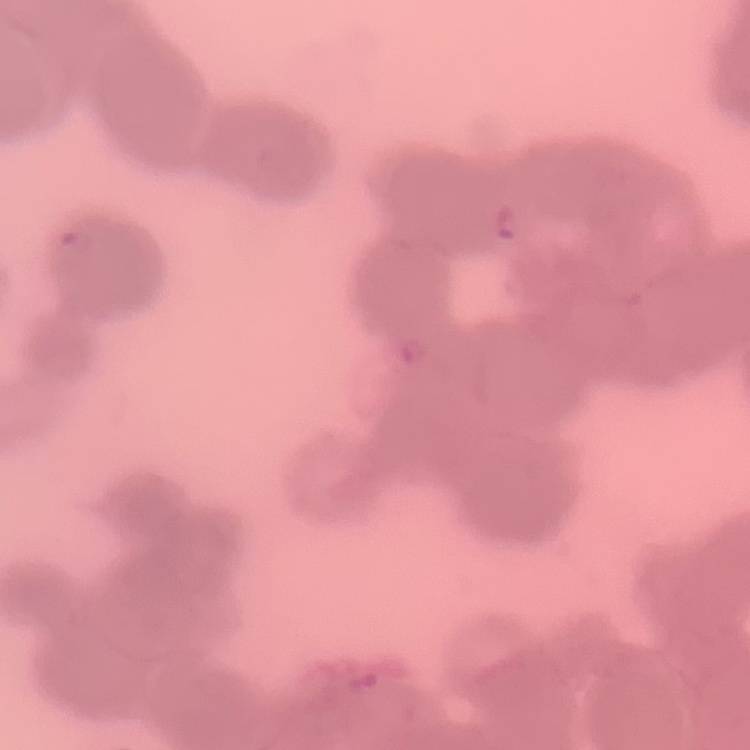
red_blood_cell_morphology: rouleaux formation
preparation: thin peripheral smear
image_type: square crop of a larger photomicrograph
stain: Field's or Giemsa